Classify this cell by malaria status.
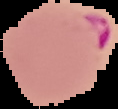

Parasitized.

Image is 118×109 pixels. The area outside the segmented cell region is set to black. From a thin blood smear.